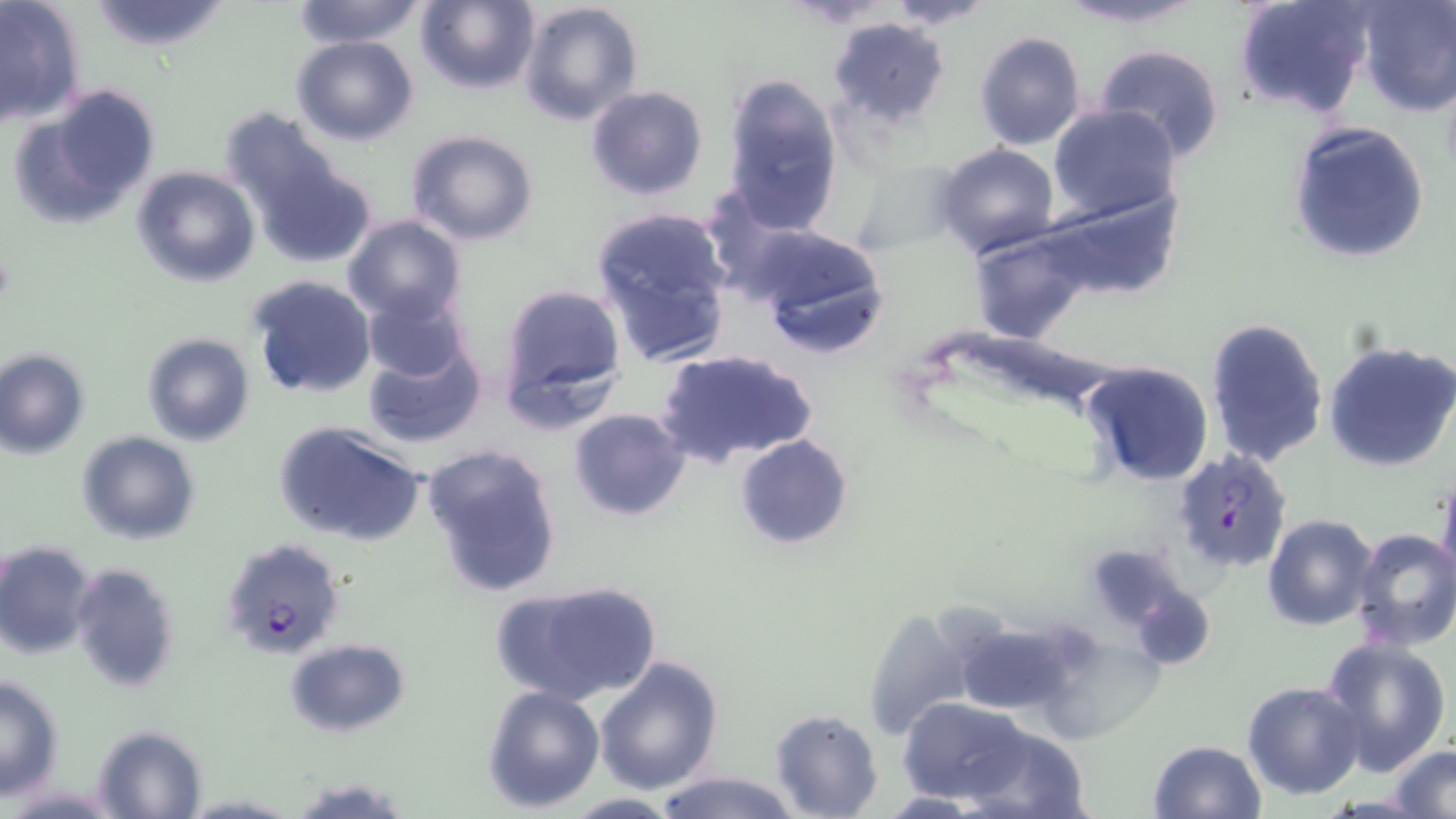
plasmodium_falciparum_infected_red_blood_cell_locations: 'approximate bounding boxes as (x1,y1)-(x2,y2) corner pairs in pixels: (1171,449)-(1295,574), (221,537)-(345,658)'
slide_level_diagnosis: Plasmodium falciparum
field_of_view: one of a larger specimen
uninfected_red_blood_cell_locations: 'approximate bounding boxes as (x1,y1)-(x2,y2) corner pairs in pixels: (0,0)-(87,127), (87,0)-(231,54), (290,0)-(425,47), (414,0)-(540,94), (880,0)-(1000,29), (1055,0)-(1207,28), (1231,0)-(1375,121), (517,1)-(644,127), (1355,1)-(1455,117), (826,17)-(950,128), (973,31)-(1087,151), (291,36)-(419,146), (1093,44)-(1227,165), (721,75)-(844,231), (15,83)-(162,224), (585,84)-(708,202), (1048,105)-(1181,221), (1287,121)-(1432,266), (236,124)-(373,270), (405,129)-(542,245), (933,144)-(1059,261), (850,159)-(958,257), (131,166)-(260,286), (1038,184)-(1182,300), (588,207)-(735,368), (342,214)-(468,327), (746,223)-(891,359), (971,231)-(1095,342), (245,274)-(378,399), (497,282)-(628,423), (362,291)-(470,385), (1204,318)-(1329,469), (141,331)-(256,447), (362,336)-(487,448), (1323,340)-(1456,472), (657,348)-(817,470), (0,349)-(89,458), (1077,358)-(1215,488), (568,407)-(691,520), (273,418)-(428,548), (75,430)-(200,545), (734,434)-(852,550), (421,441)-(564,599), (1436,475)-(1456,595), (1262,514)-(1379,630), (1348,527)-(1456,651), (0,540)-(97,660), (69,561)-(180,692), (493,578)-(662,704), (860,607)-(978,743), (967,627)-(1075,719), (1051,627)-(1168,745), (1319,636)-(1452,776), (285,638)-(411,737), (594,657)-(724,795), (0,675)-(63,798), (1243,681)-(1365,802), (480,683)-(605,813), (898,698)-(1032,804), (769,709)-(882,819), (91,725)-(207,818), (960,726)-(1092,819), (1148,739)-(1268,819), (1390,745)-(1456,817), (651,769)-(801,819), (290,774)-(414,817), (875,791)-(993,817), (179,793)-(300,818), (557,793)-(685,818)'
preparation: thin blood smear
stain: May-Grünwald-Giemsa
magnification: 1000x
image_size: 1456×819 pixels
modality: optical microscopy